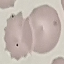

Summary:
  - Result: no malaria parasites detected
  - Preparation: thin blood smear
  - Image type: automatically extracted cell patch, resized to 64 × 64 pixels
  - Stain: Giemsa
  - Capture: smartphone through the microscope eyepiece